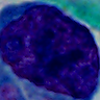

Photomicrograph. 1000x magnification. A leukocyte is seen.